Comment on the morphology of the red blood cells.
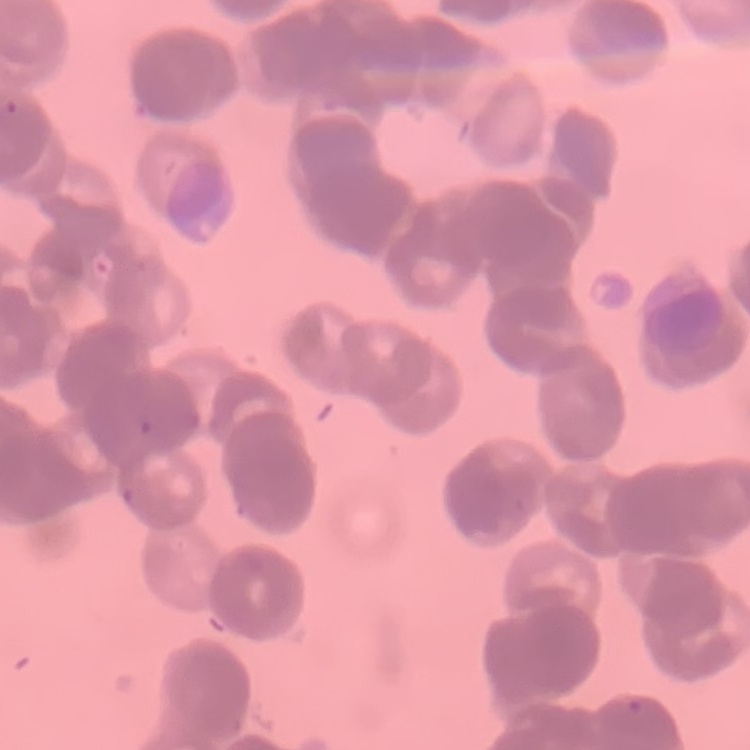
Rouleaux formation.

Thin peripheral smear. One tile cut from a larger photomicrograph. Field's or Giemsa stain.